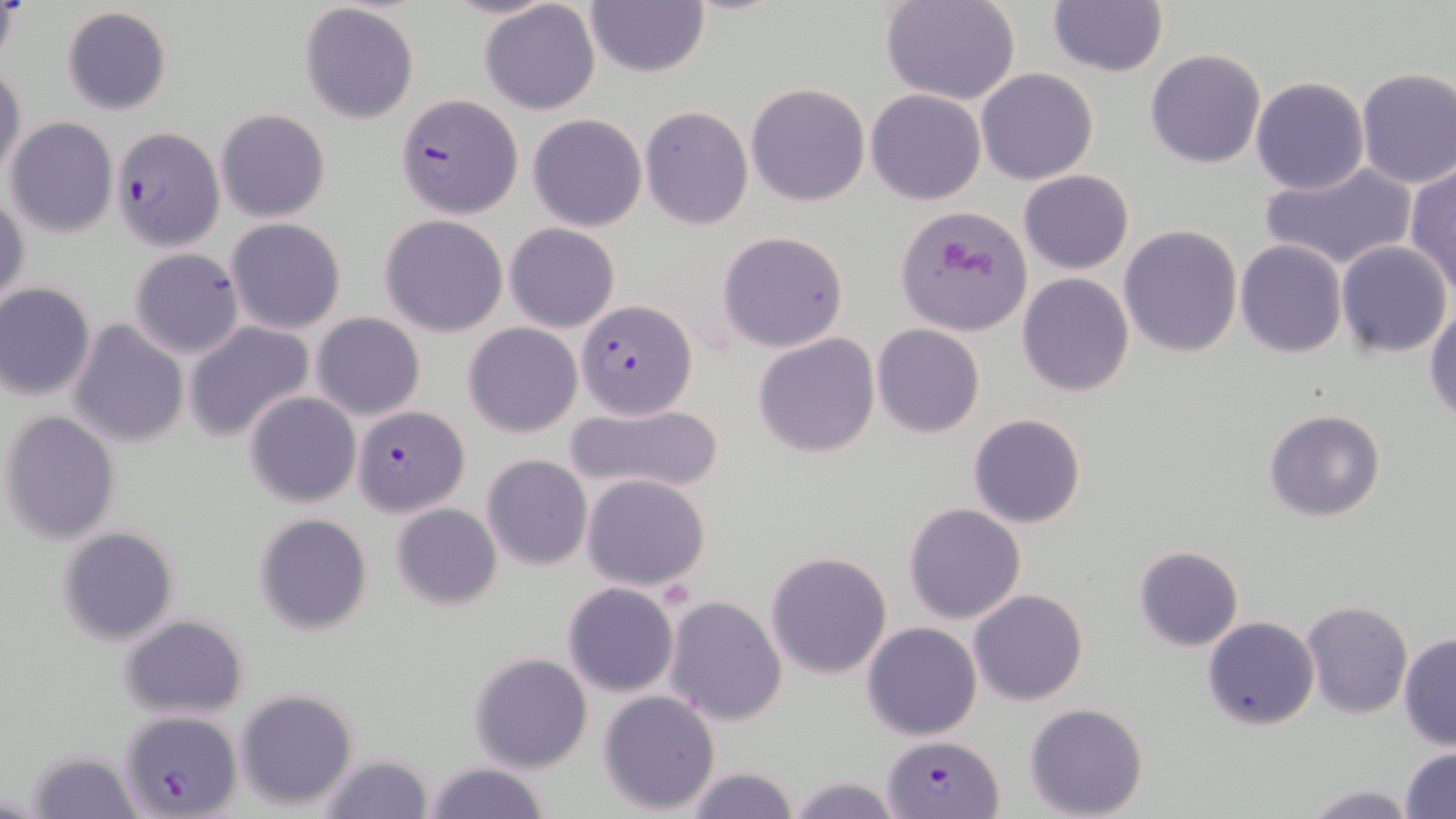

slide_level_diagnosis: Plasmodium falciparum
preparation: thin blood film
modality: optical microscopy
uninfected_red_blood_cell_locations: 'approximate bounding boxes as (x1, y1, x2, y2) in pixels: (0, 0, 23, 72), (584, 0, 710, 79), (881, 0, 1021, 105), (299, 2, 419, 123), (479, 2, 601, 115), (1047, 2, 1168, 78), (60, 7, 172, 115), (1145, 49, 1267, 168), (0, 63, 25, 184), (1355, 66, 1456, 189), (976, 68, 1100, 185), (1251, 76, 1369, 195), (746, 83, 870, 207), (866, 89, 985, 205), (640, 106, 752, 230), (216, 109, 330, 222), (527, 113, 647, 232), (6, 117, 117, 237), (1258, 160, 1417, 273), (1405, 162, 1456, 294), (1018, 170, 1133, 275), (1, 192, 28, 311), (897, 206, 1030, 336), (380, 213, 508, 337), (226, 218, 347, 334), (504, 223, 620, 333), (1120, 224, 1242, 359), (718, 230, 850, 353), (1336, 240, 1452, 357), (1234, 241, 1346, 357), (129, 248, 244, 358), (1016, 274, 1135, 396), (0, 281, 96, 400), (1426, 306, 1456, 421), (311, 311, 426, 421), (68, 319, 190, 448), (185, 322, 315, 442), (464, 322, 581, 437), (871, 323, 986, 437), (753, 333, 880, 458), (244, 391, 360, 507), (566, 400, 724, 496), (1263, 408, 1386, 522), (2, 410, 122, 543), (968, 413, 1087, 528), (481, 454, 592, 571), (581, 473, 711, 591), (390, 502, 502, 610), (903, 502, 1028, 623), (254, 514, 372, 636), (57, 527, 179, 645), (1132, 544, 1244, 651), (765, 551, 894, 678), (561, 582, 681, 698), (969, 589, 1088, 706), (661, 595, 787, 726), (1301, 601, 1412, 718), (118, 613, 250, 720), (1202, 616, 1320, 731), (861, 622, 982, 739), (1398, 633, 1455, 750), (469, 652, 594, 773), (233, 688, 360, 811), (597, 689, 721, 814), (1024, 702, 1150, 818), (1398, 746, 1456, 819), (25, 749, 145, 819), (316, 753, 435, 819), (422, 761, 551, 819), (681, 765, 800, 819), (784, 777, 908, 819), (1300, 784, 1422, 818)'
plasmodium_falciparum_infected_red_blood_cell_locations: 'approximate bounding boxes as (x1, y1, x2, y2) in pixels: (396, 93, 521, 219), (111, 127, 224, 252), (577, 299, 697, 420), (353, 403, 468, 515), (118, 708, 243, 816), (881, 735, 1004, 818)'
magnification: 1000x
field_of_view: one of a larger specimen
platelet_locations: 'approximate bounding boxes as (x1, y1, x2, y2) in pixels: (936, 241, 1000, 283)'
image_size: 1456×819 pixels
stain: May-Grünwald-Giemsa